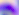 Toxoplasma gondii is seen. 400x magnification. Micrograph.